Name the cell type shown.
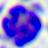

A leukocyte.

modality: photomicrograph
magnification: 400x